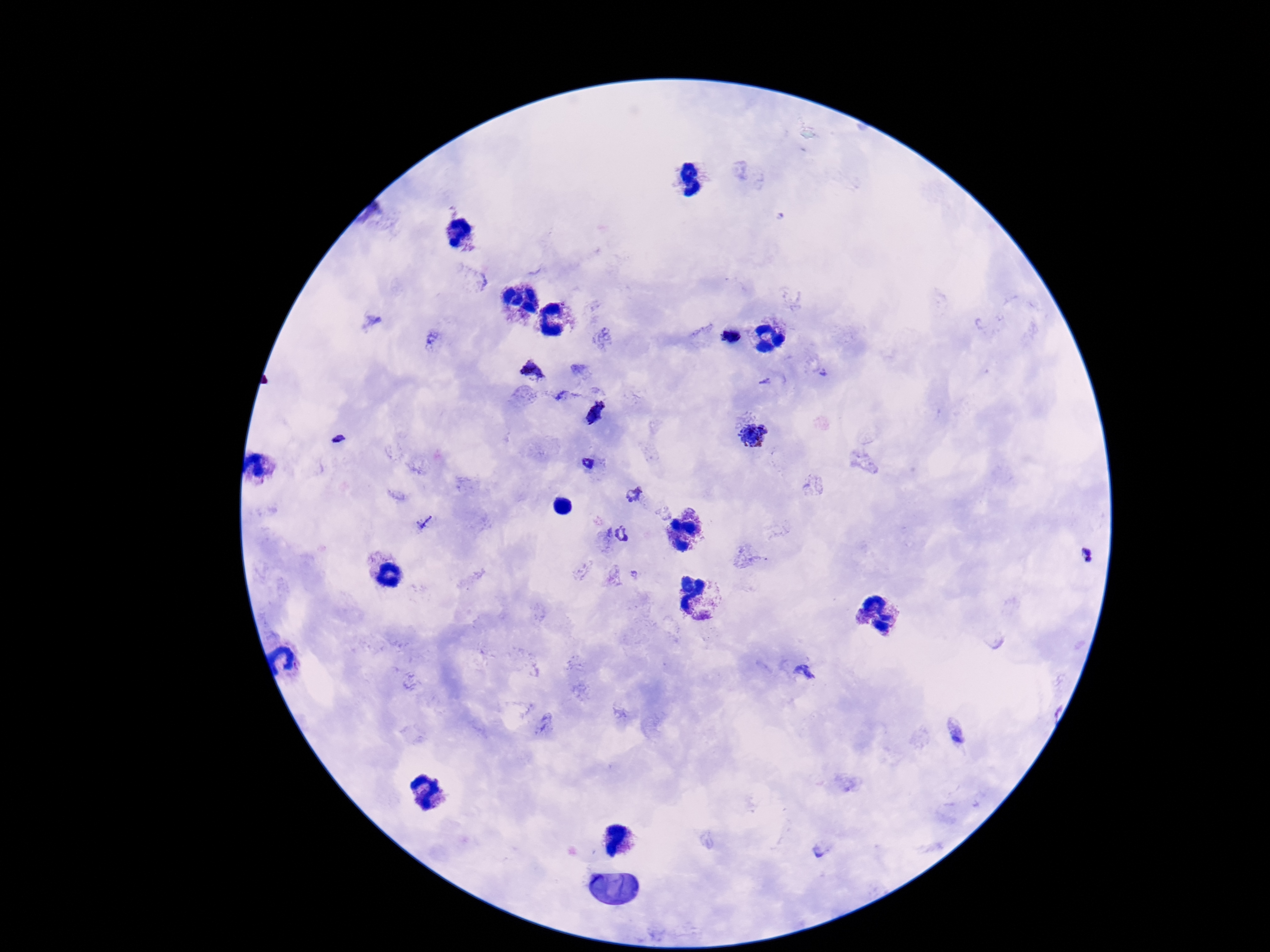

field of view = single
magnification = 100x
image size = 1270×952 pixels
Plasmodium parasite locations = approximate object centers, in pixels from the top-left corner: (x=732, y=334), (x=534, y=372), (x=562, y=397), (x=596, y=412), (x=753, y=435), (x=336, y=439), (x=589, y=462), (x=633, y=495), (x=425, y=523), (x=620, y=535), (x=1088, y=556), (x=804, y=672), (x=959, y=733), (x=821, y=849)
preparation = thick blood smear
patient malaria status = infected
stain = Giemsa
capture = smartphone camera through the microscope eyepiece